State the blood parasite species.
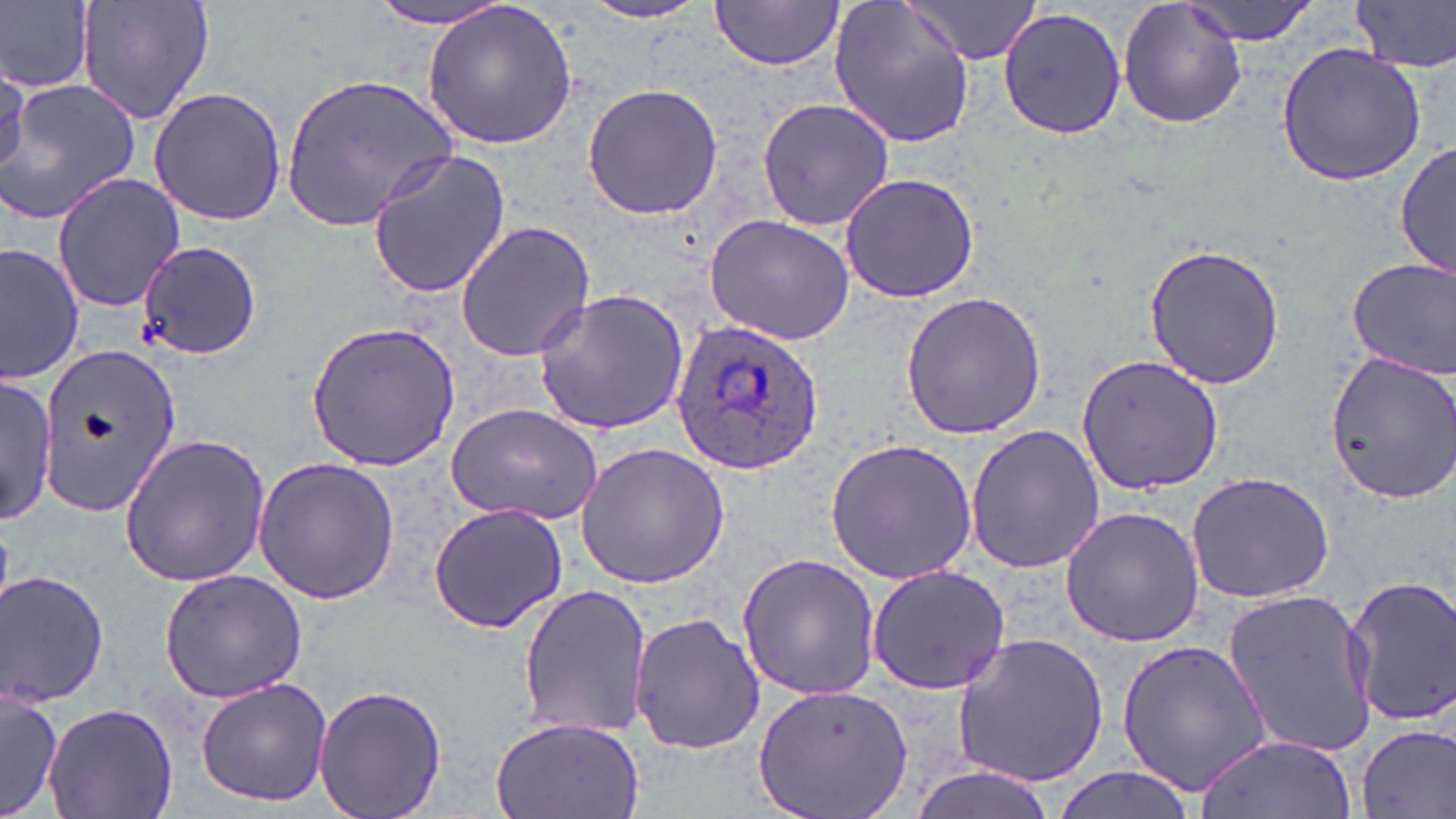

Plasmodium ovale.

Summary:
  - Coordinate format: approximate bounding boxes as named x1/y1/x2/y2 corners in pixels
  - Uninfected red blood cell locations: (x1=2, y1=0, x2=96, y2=93), (x1=76, y1=0, x2=215, y2=125), (x1=372, y1=0, x2=521, y2=32), (x1=709, y1=0, x2=846, y2=70), (x1=826, y1=0, x2=979, y2=150), (x1=1117, y1=0, x2=1248, y2=130), (x1=1182, y1=0, x2=1320, y2=44), (x1=1350, y1=0, x2=1456, y2=74), (x1=420, y1=1, x2=580, y2=152), (x1=901, y1=1, x2=1040, y2=66), (x1=579, y1=2, x2=711, y2=24), (x1=998, y1=7, x2=1128, y2=140), (x1=1275, y1=42, x2=1428, y2=187), (x1=0, y1=63, x2=26, y2=179), (x1=280, y1=70, x2=457, y2=233), (x1=1, y1=77, x2=141, y2=223), (x1=581, y1=83, x2=724, y2=219), (x1=148, y1=87, x2=288, y2=226), (x1=756, y1=97, x2=895, y2=232), (x1=1394, y1=141, x2=1454, y2=281), (x1=365, y1=150, x2=513, y2=300), (x1=50, y1=171, x2=187, y2=312), (x1=838, y1=171, x2=980, y2=304), (x1=704, y1=214, x2=855, y2=344), (x1=454, y1=221, x2=596, y2=362), (x1=1, y1=241, x2=86, y2=384), (x1=138, y1=242, x2=262, y2=360), (x1=1142, y1=242, x2=1286, y2=389), (x1=1347, y1=257, x2=1455, y2=379), (x1=531, y1=288, x2=691, y2=437), (x1=899, y1=291, x2=1050, y2=441), (x1=305, y1=322, x2=461, y2=472), (x1=35, y1=340, x2=184, y2=517), (x1=1323, y1=352, x2=1456, y2=503), (x1=1076, y1=355, x2=1223, y2=493), (x1=0, y1=372, x2=56, y2=526), (x1=444, y1=403, x2=604, y2=524), (x1=964, y1=424, x2=1103, y2=574), (x1=117, y1=432, x2=271, y2=588), (x1=824, y1=438, x2=980, y2=585), (x1=573, y1=442, x2=730, y2=589), (x1=253, y1=456, x2=402, y2=606), (x1=1184, y1=471, x2=1337, y2=605), (x1=427, y1=501, x2=569, y2=634), (x1=1059, y1=505, x2=1207, y2=648), (x1=737, y1=553, x2=883, y2=700), (x1=866, y1=563, x2=1010, y2=695), (x1=0, y1=569, x2=111, y2=710), (x1=157, y1=570, x2=308, y2=701), (x1=1343, y1=573, x2=1456, y2=729), (x1=517, y1=585, x2=654, y2=741), (x1=1224, y1=587, x2=1381, y2=760), (x1=629, y1=613, x2=766, y2=756), (x1=951, y1=633, x2=1110, y2=787), (x1=1115, y1=638, x2=1273, y2=795), (x1=195, y1=676, x2=335, y2=807), (x1=312, y1=683, x2=447, y2=819), (x1=1, y1=685, x2=65, y2=819), (x1=750, y1=686, x2=917, y2=819), (x1=43, y1=702, x2=178, y2=819), (x1=489, y1=715, x2=647, y2=819), (x1=1354, y1=724, x2=1455, y2=818), (x1=1197, y1=733, x2=1357, y2=819), (x1=1043, y1=768, x2=1198, y2=819)
  - Plasmodium ovale-infected red blood cell locations: (x1=668, y1=318, x2=824, y2=476)
  - Image size: 1456×819 pixels
  - Stain: May-Grünwald-Giemsa
  - Field of view: single
  - Preparation: thin blood film
  - Magnification: 1000x
  - Modality: optical microscopy